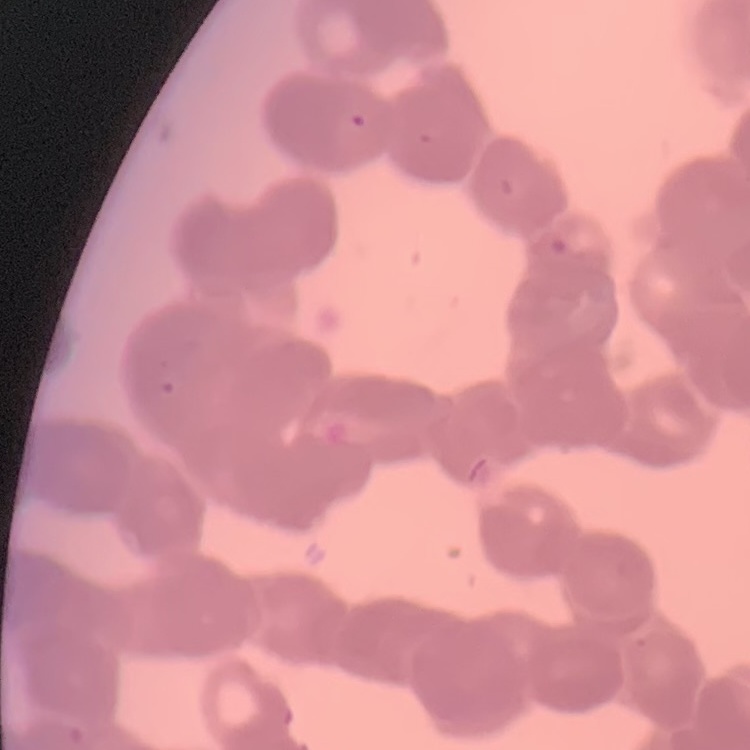
Summary:
  - Erythrocyte morphology: rouleaux formation
  - Stain: Field's or Giemsa
  - Image type: one tile cut from a larger photomicrograph
  - Preparation: thin blood film